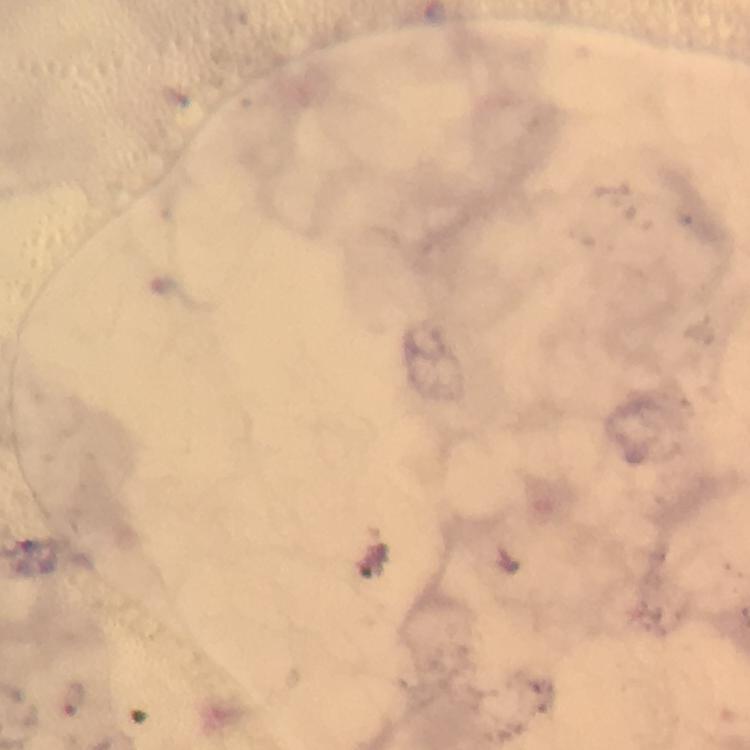

Approximate centers as (x, y) in pixels.
Summary:
  - Malaria parasite locations: (73, 700)
  - Preparation: thick blood smear
  - Image size: 750×750 pixels
  - Immersion oil: applied
  - Capture: smartphone mounted on the microscope
  - Stain: Giemsa
  - Cropped from: a single field of view
  - Context: from a malaria diagnostic workup
  - Magnification: 100x